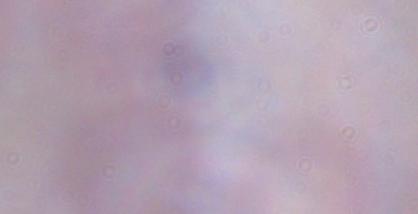
Summary:
  - Identification: trypanosome
  - Modality: micrograph
  - Magnification: 1000x